Assess this cell for malaria.
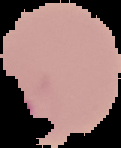

It is parasitized.

image size = 121×148 pixels
preparation = thin blood film
image type = segmented cell region on a black background